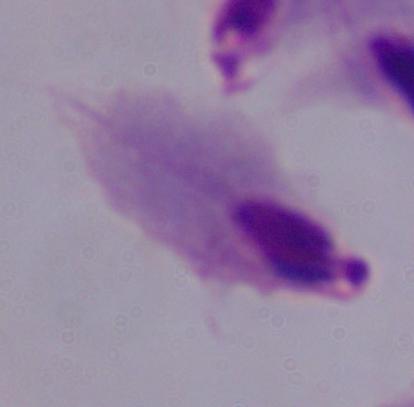
Photomicrograph. A trichomonad is shown. 1000x magnification.